Point out each Plasmodium parasite.
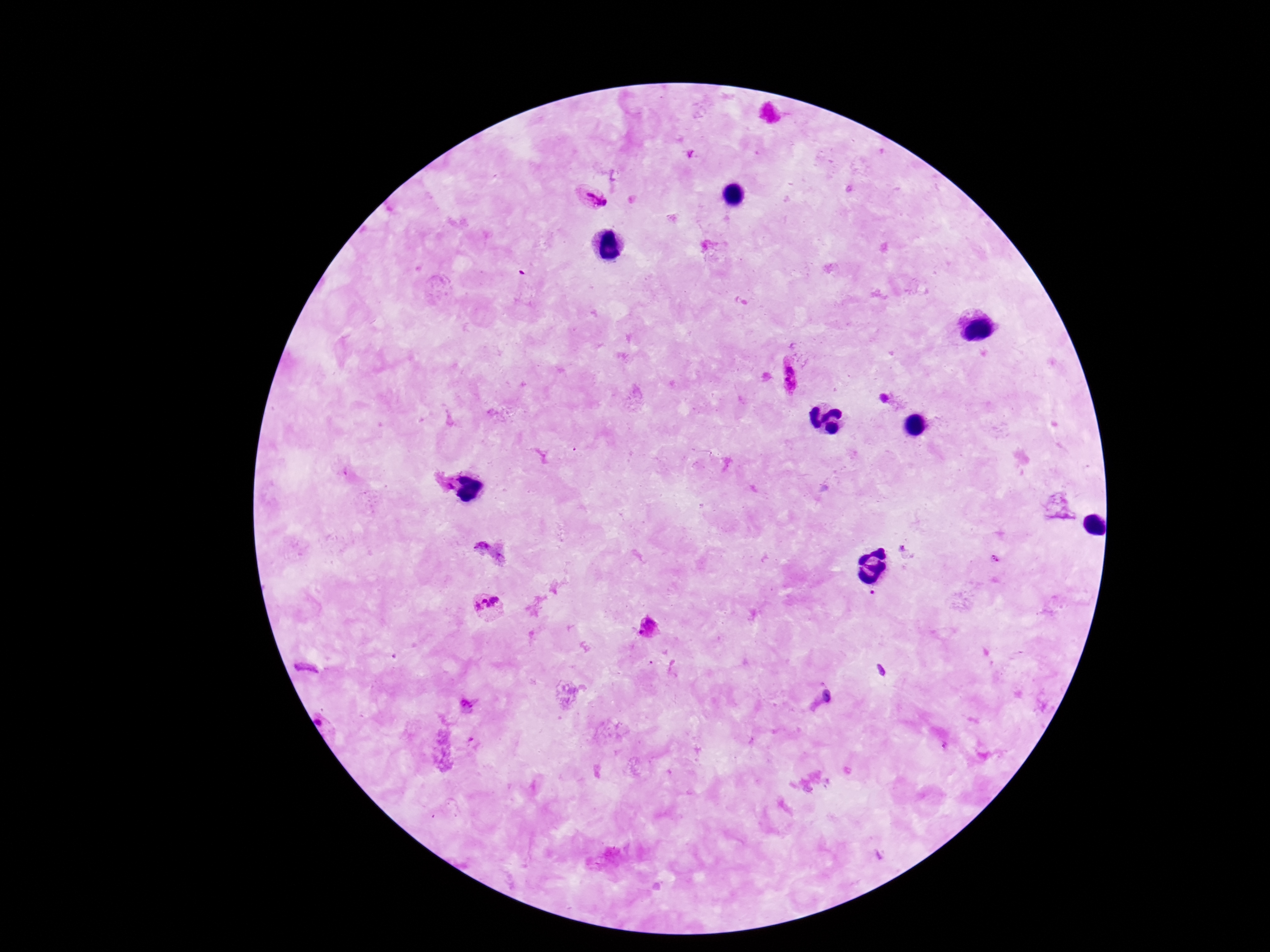
Approximate centers as [x, y] in pixels.
Plasmodium parasites: [590, 196], [790, 378], [886, 398], [480, 548], [489, 605], [648, 627], [307, 669], [466, 705], [320, 722].

image size = 1270×952 pixels
preparation = thick blood film
field of view = one from this slide
patient malaria status = positive
capture = smartphone camera through the microscope eyepiece
magnification = 100x
stain = Giemsa